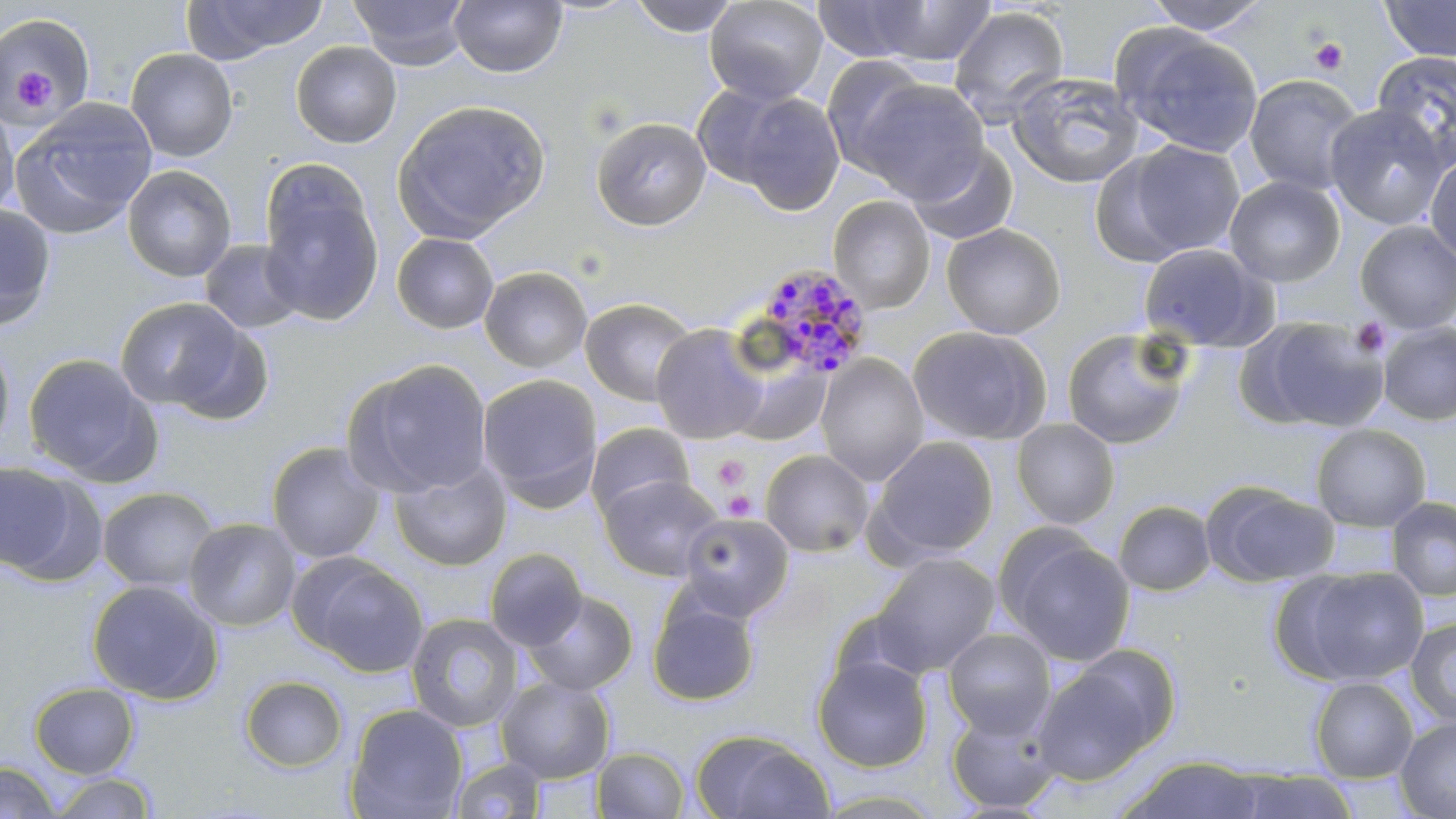
Summary:
  - Coordinate format: approximate bounding boxes as [x1, y1, x2, y2] in pixels
  - Platelet locations: [1308, 37, 1348, 76], [10, 70, 58, 113], [1349, 316, 1391, 357], [714, 455, 751, 491], [721, 490, 757, 520]
  - Plasmodium malariae-infected red blood cell locations: [751, 262, 874, 380]
  - Uninfected red blood cell locations: [349, 0, 471, 69], [449, 0, 567, 78], [629, 0, 740, 37], [704, 0, 828, 105], [1140, 0, 1275, 35], [1379, 0, 1456, 62], [181, 1, 328, 62], [812, 1, 934, 63], [868, 1, 999, 67], [948, 6, 1070, 127], [0, 12, 96, 121], [1112, 25, 1265, 158], [291, 41, 401, 148], [125, 48, 238, 162], [1373, 48, 1456, 167], [821, 56, 935, 175], [1007, 71, 1146, 189], [1243, 74, 1365, 196], [851, 77, 990, 200], [691, 82, 803, 193], [733, 92, 846, 216], [0, 98, 20, 222], [11, 99, 158, 239], [393, 99, 550, 242], [1324, 104, 1451, 230], [591, 116, 711, 231], [1111, 139, 1248, 263], [907, 142, 1019, 247], [1425, 153, 1456, 265], [122, 164, 236, 282], [259, 171, 385, 325], [1224, 176, 1345, 287], [828, 195, 935, 313], [0, 204, 57, 331], [1355, 221, 1456, 333], [941, 223, 1066, 339], [391, 233, 499, 334], [200, 239, 306, 335], [1138, 242, 1274, 351], [479, 266, 592, 373], [114, 297, 254, 415], [580, 297, 698, 407], [1242, 316, 1388, 432], [1378, 322, 1456, 426], [651, 324, 770, 444], [908, 325, 1051, 445], [1061, 327, 1193, 450], [0, 334, 16, 459], [23, 352, 158, 483], [815, 354, 929, 485], [729, 358, 830, 447], [344, 359, 493, 498], [477, 374, 602, 507], [1011, 418, 1120, 529], [585, 422, 697, 520], [1311, 424, 1431, 532], [868, 436, 1000, 561], [266, 441, 387, 564], [760, 449, 874, 557], [388, 459, 511, 571], [0, 460, 85, 579], [599, 474, 723, 581], [1202, 482, 1339, 588], [96, 486, 219, 594], [1387, 497, 1456, 601], [1113, 500, 1216, 595], [679, 512, 795, 621], [183, 517, 302, 632], [998, 529, 1137, 668], [484, 548, 588, 651], [870, 552, 1001, 676], [294, 553, 429, 677], [1283, 566, 1429, 686], [87, 579, 223, 704], [523, 590, 639, 696], [647, 590, 760, 707], [406, 612, 524, 733], [1405, 617, 1456, 727], [942, 628, 1056, 739], [1032, 652, 1171, 785], [812, 653, 933, 773], [240, 675, 348, 772], [496, 677, 615, 783], [1310, 677, 1418, 782], [29, 682, 139, 778], [344, 703, 468, 818], [946, 706, 1062, 814], [1395, 717, 1456, 819], [691, 729, 834, 818], [592, 746, 691, 818], [1117, 755, 1268, 818], [449, 757, 548, 819], [0, 761, 61, 819], [1228, 769, 1361, 818], [47, 772, 158, 818]
  - Slide-level diagnosis: Plasmodium malariae
  - Image size: 1456×819 pixels
  - Preparation: thin blood smear
  - Stain: May-Grünwald-Giemsa
  - Magnification: 1000x
  - Field of view: single
  - Modality: light microscopy